Give the extent of all Plasmodium ovale-infected red blood cells.
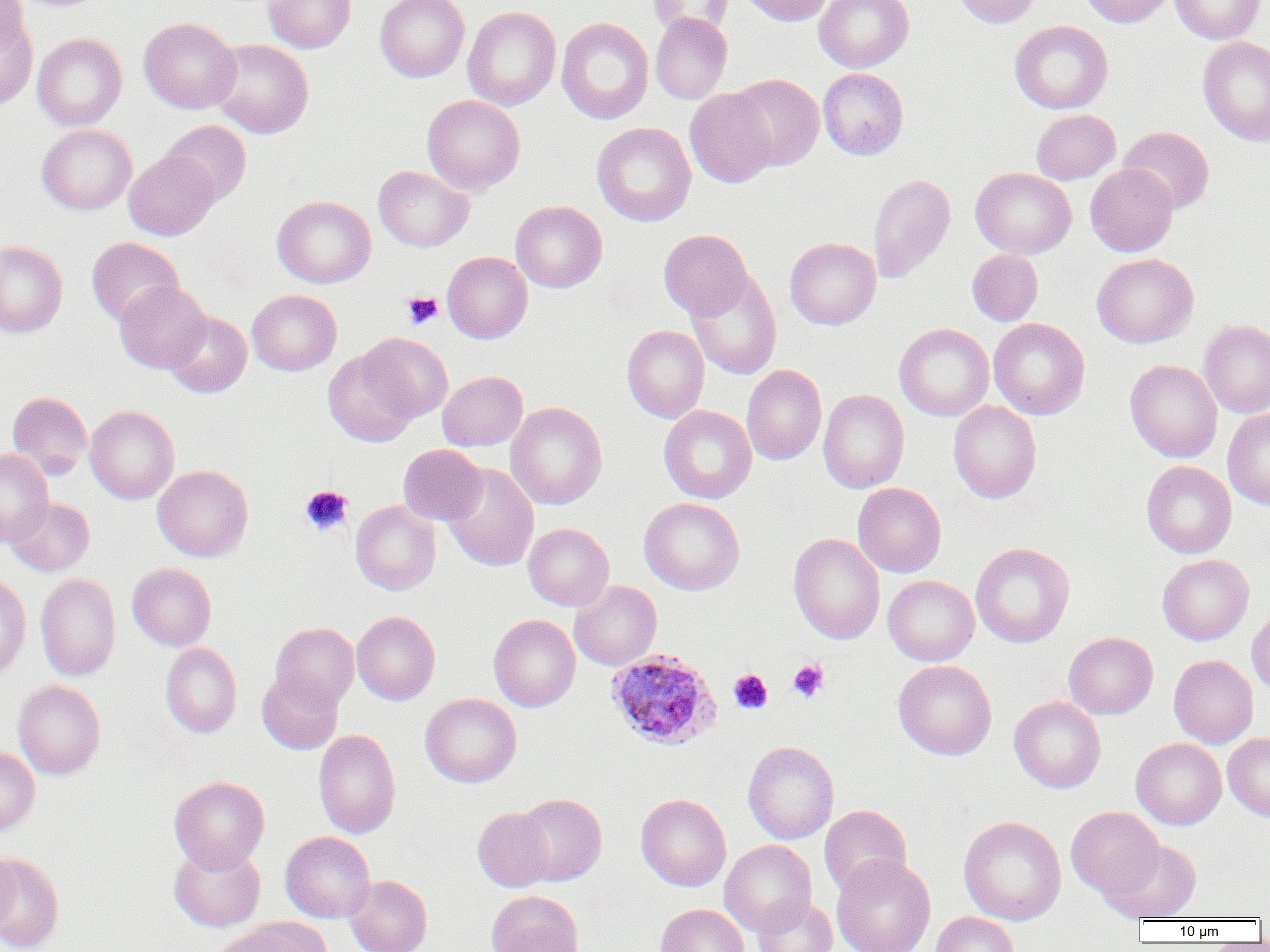
Approximate bounding boxes as (x1,y1)-(x2,y2) corner pairs in pixels.
Plasmodium ovale-infected red blood cells: (605,648)-(721,751).

Uninfected red blood cell locations: (0,0)-(28,56), (10,0)-(111,13), (262,0)-(356,53), (375,0)-(470,82), (648,0)-(733,36), (739,0)-(833,26), (814,0)-(913,73), (952,0)-(1042,28), (1079,0)-(1174,27), (1170,0)-(1265,44), (462,6)-(561,111), (0,9)-(38,111), (650,12)-(732,104), (138,17)-(241,114), (556,17)-(654,124), (1009,20)-(1113,114), (31,33)-(127,131), (1197,36)-(1270,147), (208,38)-(314,139), (818,67)-(909,160), (729,73)-(824,171), (684,88)-(778,188), (422,94)-(525,196), (1031,109)-(1120,184), (160,120)-(252,206), (592,122)-(695,227), (36,124)-(137,215), (1118,126)-(1215,214), (124,150)-(218,240), (1085,164)-(1178,257), (373,165)-(474,252), (971,168)-(1077,258), (867,173)-(956,283), (273,195)-(376,288), (511,200)-(607,293), (659,229)-(754,320), (86,237)-(184,327), (785,237)-(881,329), (0,240)-(68,338), (966,249)-(1043,326), (442,251)-(533,343), (1092,253)-(1198,348), (687,269)-(782,380), (114,281)-(211,373), (247,289)-(342,376), (163,309)-(252,398), (988,317)-(1090,419), (1199,319)-(1270,418), (894,323)-(994,421), (622,324)-(710,423), (360,333)-(453,422), (323,347)-(420,447), (1124,359)-(1222,463), (741,364)-(827,465), (438,370)-(528,451), (818,389)-(909,494), (7,391)-(92,480), (948,400)-(1041,504), (505,401)-(607,510), (659,404)-(757,504), (85,405)-(180,504), (1222,408)-(1270,510), (398,444)-(486,525), (0,449)-(53,546), (1141,460)-(1236,559), (442,463)-(539,572), (152,464)-(253,562), (853,483)-(946,577), (5,497)-(95,576), (639,497)-(745,595), (350,499)-(441,595), (523,522)-(614,610), (788,532)-(885,645), (970,542)-(1075,648), (1157,554)-(1254,645), (127,562)-(216,651), (0,571)-(32,682), (35,573)-(120,681), (883,575)-(979,665), (569,580)-(662,671), (1247,606)-(1270,698), (352,611)-(440,705), (489,614)-(581,712), (271,621)-(359,710), (1063,632)-(1158,719), (161,642)-(242,738), (1169,654)-(1258,748), (893,659)-(997,760), (257,670)-(343,755), (13,680)-(106,780), (420,692)-(522,787), (1009,696)-(1106,793), (313,729)-(401,838), (1223,733)-(1270,821), (1130,738)-(1227,830), (742,740)-(839,844), (0,746)-(40,837), (169,775)-(270,873), (515,793)-(607,886), (636,793)-(732,891), (819,804)-(912,897), (1066,806)-(1164,900), (472,807)-(556,892), (958,816)-(1067,925), (280,831)-(375,923), (1102,839)-(1201,922), (719,840)-(817,936), (169,843)-(266,932), (0,846)-(16,940), (1,851)-(65,952), (832,854)-(936,952), (344,874)-(432,952), (486,890)-(584,952), (751,896)-(837,952), (655,903)-(750,952), (930,912)-(1019,952), (235,916)-(334,951), (207,925)-(306,952). Platelet locations: (401,291)-(443,329), (299,485)-(354,536), (788,659)-(829,702), (728,669)-(773,714). Slide-level diagnosis: Plasmodium ovale. Light microscopy. Single field of view. Image is 1270×952 pixels. Thin blood smear. Captured at 1000x magnification.